Report the malaria status of this cell.
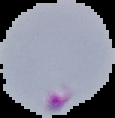
Parasitized.

image size = 115×118 pixels
image type = segmented cell region with the area outside set to black
preparation = thin blood film